Classify this cell by malaria status.
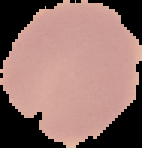
Uninfected.

image size = 142×148 pixels
preparation = thin blood film
image type = cell region segmented out of the field of view; surrounding area masked to black